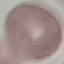

result = no malaria parasites detected
stain = Giemsa
image type = automatically extracted cell patch, resized to 64 × 64 pixels
preparation = thin smear
capture = smartphone camera at the microscope eyepiece